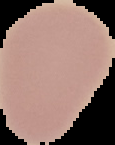 The area outside the segmented cell region is set to black. From a thin blood film. Image is 115×145 pixels. Malaria status: uninfected.